Classify this cell by malaria status.
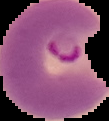
It is parasitized.

image_type: segmented cell region on a black background
preparation: thin blood film
image_size: 109×121 pixels